Assess this cell for malaria.
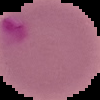
It is parasitized.

preparation = thin blood film
image size = 100×100 pixels
image type = cell region segmented out of the field of view; surrounding area masked to black